Assess the morphology of the erythrocytes.
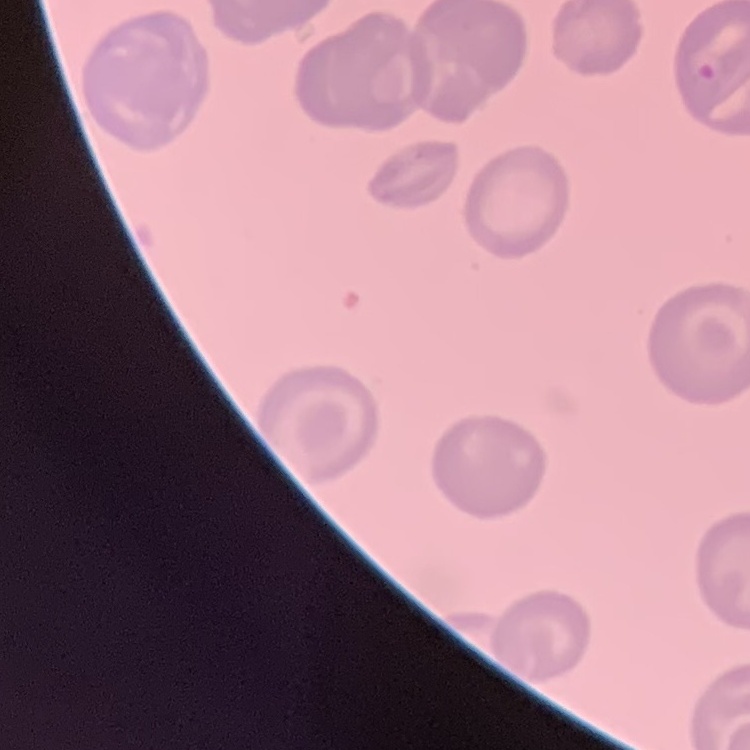
They show no rouleaux formation.

stain = Field's or Giemsa
preparation = thin peripheral smear
image type = square crop of a larger photomicrograph